Classify this cell by malaria status.
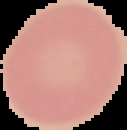

It is uninfected.

Summary:
  - Image type: cell region segmented out of the field of view; surrounding area masked to black
  - Preparation: thin blood film
  - Image size: 127×130 pixels